Classify this cell by malaria status.
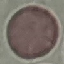

Uninfected.

Summary:
  - Preparation: thin smear
  - Stain: Giemsa
  - Capture: smartphone through the microscope eyepiece
  - Image type: automatically extracted cell patch, resized to 64 × 64 pixels